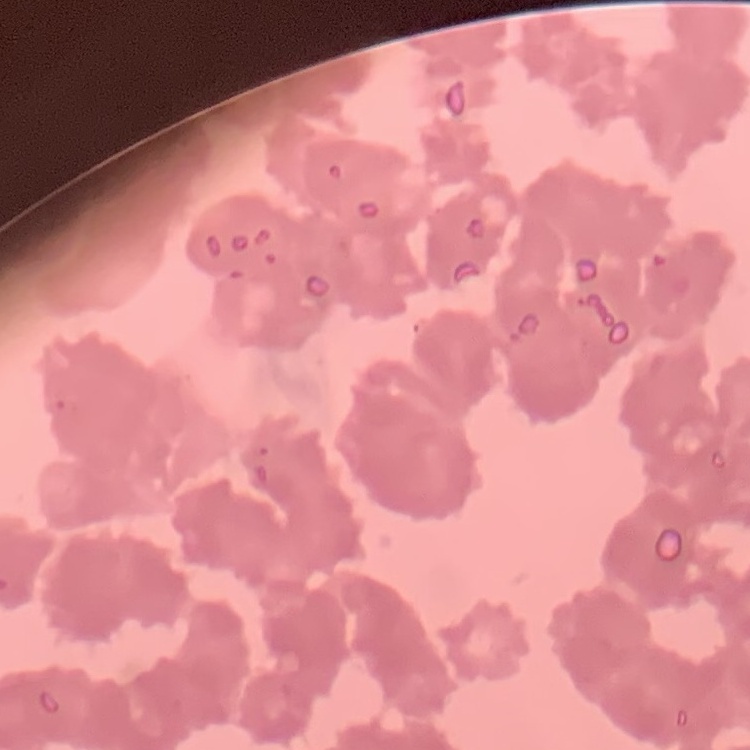
erythrocyte morphology = rouleaux formation
image type = square crop of a larger photomicrograph
stain = Field's or Giemsa
preparation = thin blood smear